Locate every P. falciparum parasite and identify its life-cycle stage.
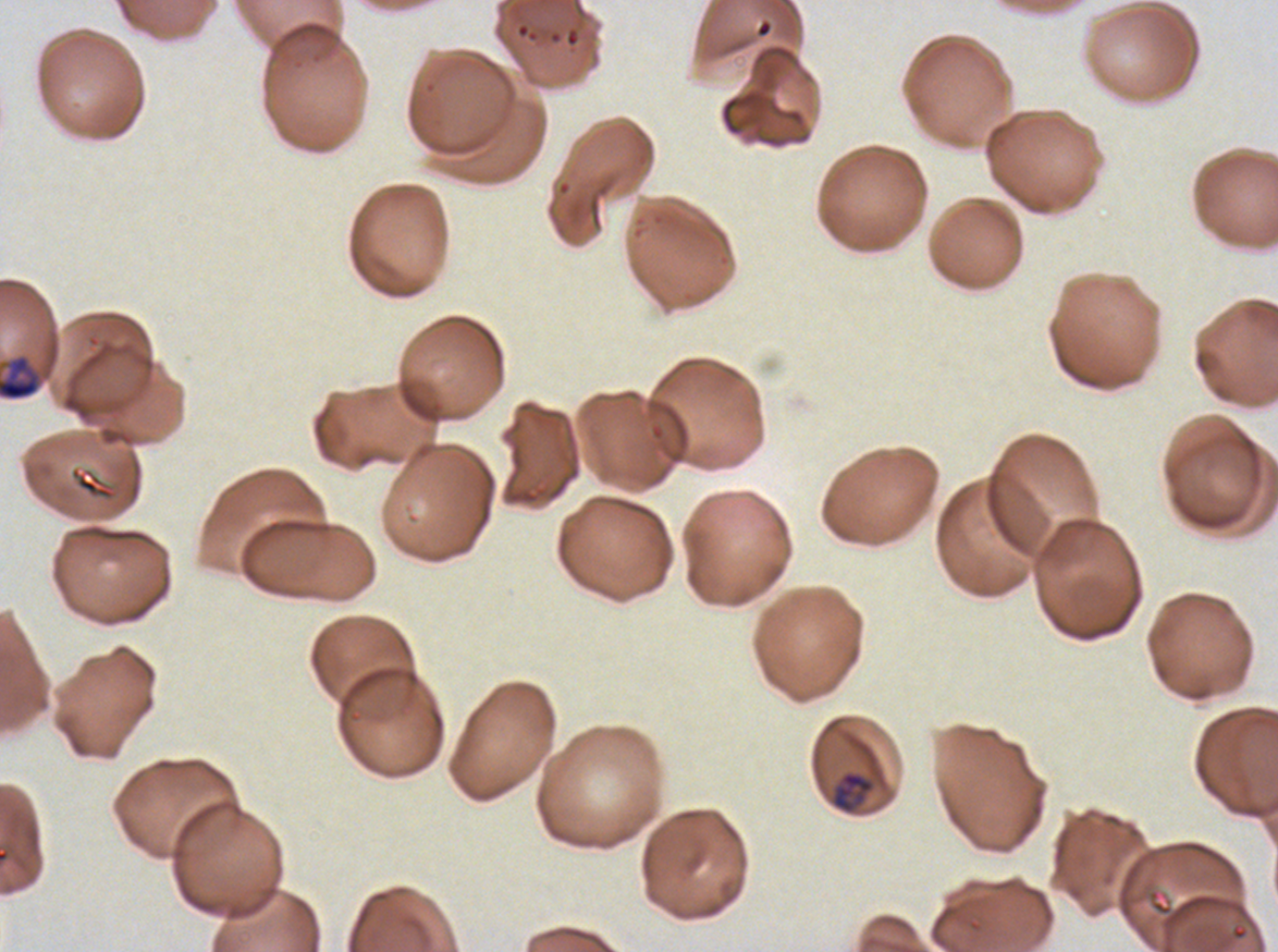
Approximate bounding rectangles given as corner coordinates in pixels from the top-left.
Late-ring/early-trophozoite forms: (x1=830, y1=770, x2=875, y2=814).
Late trophozoites: (x1=0, y1=353, x2=43, y2=401).
No rings, mid trophozoites, early schizonts, late schizonts, segmenters, or gametocytes observed.

Summary:
  - Specimen: P. falciparum cultured ex vivo for 24 to 48 hours, from a patient in The Gambia
  - Life-cycle stages observed: late-ring/early-trophozoite, late trophozoite
  - Field of view: one sub-image of a larger composite
  - Stain: Giemsa
  - Preparation: thin blood film
  - Image size: 1278×952 pixels